Classify this cell by malaria status.
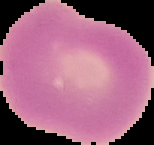

Uninfected.

{
  "image_type": "segmented cell region on a black background",
  "preparation": "thin blood smear",
  "image_size": "154×145 pixels"
}